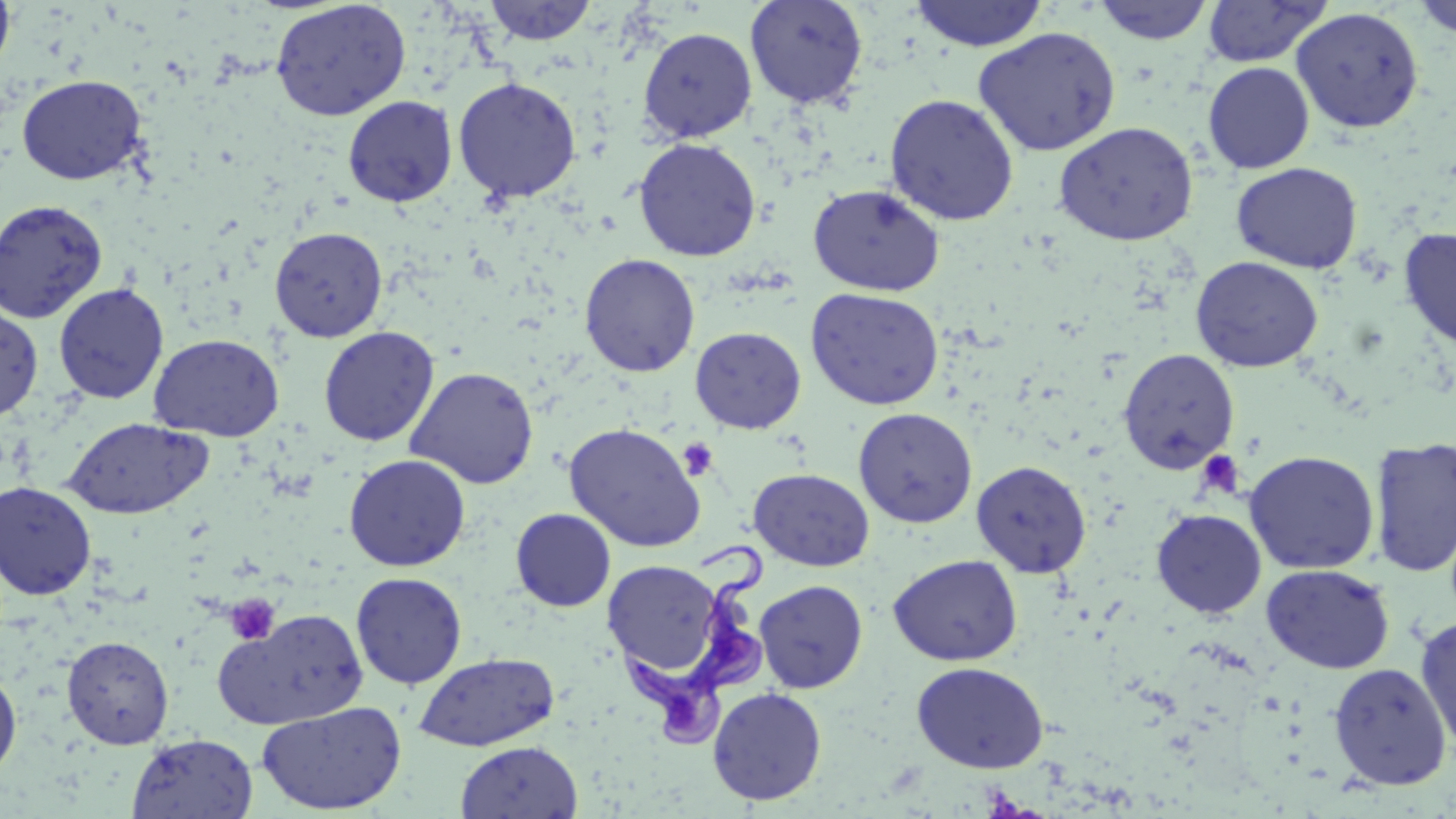
Summary:
  - Coordinate format: approximate bounding boxes as (x1, y1, x2, y2) in pixels
  - Uninfected red blood cell locations: (0, 0, 16, 79), (481, 0, 599, 46), (744, 0, 868, 109), (908, 0, 1049, 52), (1090, 0, 1215, 46), (270, 1, 412, 121), (1201, 1, 1330, 68), (1408, 1, 1456, 39), (1290, 7, 1424, 133), (972, 26, 1121, 156), (637, 27, 757, 143), (1203, 61, 1315, 174), (16, 74, 148, 185), (452, 76, 582, 203), (884, 93, 1020, 226), (342, 95, 458, 207), (1053, 121, 1199, 246), (633, 137, 762, 262), (1230, 162, 1363, 273), (807, 184, 945, 297), (0, 200, 107, 323), (1398, 226, 1456, 348), (269, 227, 388, 342), (579, 253, 701, 377), (1190, 255, 1324, 373), (53, 282, 169, 404), (805, 287, 944, 410), (0, 303, 43, 421), (318, 326, 439, 446), (689, 326, 807, 434), (148, 333, 284, 441), (1118, 348, 1240, 474), (405, 367, 540, 489), (852, 407, 978, 528), (62, 415, 214, 520), (564, 422, 706, 553), (1370, 436, 1456, 578), (1243, 450, 1380, 574), (343, 453, 471, 572), (971, 460, 1092, 578), (748, 468, 875, 572), (0, 480, 98, 599), (510, 508, 616, 612), (1151, 508, 1267, 619), (888, 553, 1022, 666), (602, 559, 726, 682), (1261, 563, 1395, 674), (350, 571, 467, 689), (754, 580, 868, 693), (216, 608, 368, 729), (1414, 614, 1456, 754), (61, 635, 174, 749), (414, 652, 559, 751), (911, 661, 1050, 773), (1328, 662, 1452, 790), (0, 667, 22, 780), (707, 686, 827, 806), (256, 701, 407, 816), (126, 733, 258, 818), (455, 741, 583, 819)
  - Trypanosoma brucei locations: (620, 538, 771, 750)
  - Platelet locations: (677, 437, 719, 481), (1194, 449, 1245, 500), (225, 594, 280, 645)
  - Slide-level diagnosis: Trypanosoma brucei
  - Image size: 1456×819 pixels
  - Magnification: 1000x
  - Preparation: thin blood film
  - Stain: May-Grünwald-Giemsa
  - Modality: optical microscopy
  - Field of view: single